Name the parasite shown.
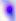
Toxoplasma gondii.

modality = photomicrograph
magnification = 400x